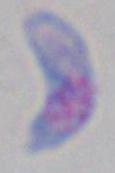

{
  "magnification": "1000x",
  "modality": "photomicrograph",
  "identification": "Toxoplasma gondii"
}